Identify the parasite.
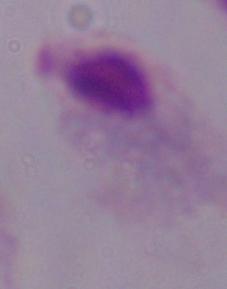

A trichomonad.

modality = micrograph
magnification = 1000x